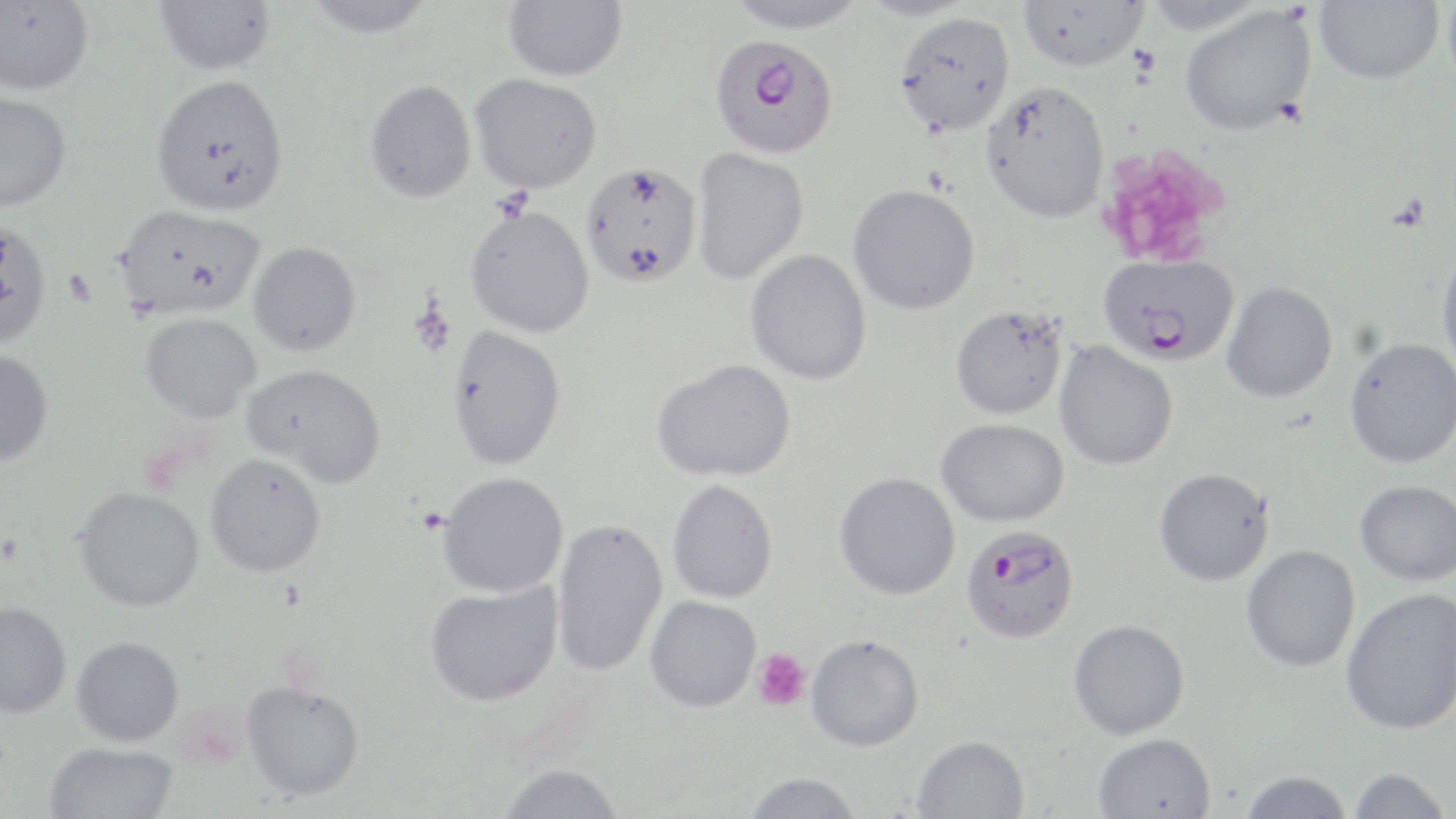

{
  "slide_level_diagnosis": "Plasmodium falciparum",
  "preparation": "thin blood smear",
  "modality": "light microscopy",
  "image_size": "1456×819 pixels",
  "plasmodium_falciparum_infected_red_blood_cell_locations": "approximate bounding boxes as (x1, y1, x2, y2) in pixels: (709, 34, 840, 159), (1098, 253, 1239, 365), (960, 524, 1080, 644)",
  "stain": "May-Grünwald-Giemsa",
  "platelet_locations": "approximate bounding boxes as (x1, y1, x2, y2) in pixels: (1098, 144, 1231, 270), (752, 648, 811, 712)",
  "uninfected_red_blood_cell_locations": "approximate bounding boxes as (x1, y1, x2, y2) in pixels: (154, 0, 275, 76), (302, 0, 436, 39), (503, 0, 627, 81), (724, 0, 869, 33), (855, 0, 979, 21), (1018, 0, 1149, 72), (1142, 0, 1267, 35), (1442, 0, 1456, 97), (0, 1, 94, 96), (1314, 1, 1444, 85), (1179, 5, 1316, 136), (893, 11, 1016, 135), (470, 73, 603, 193), (149, 74, 289, 218), (364, 80, 476, 203), (980, 81, 1110, 223), (0, 90, 72, 212), (691, 147, 809, 285), (580, 162, 703, 288), (847, 184, 981, 315), (114, 205, 265, 320), (464, 205, 595, 338), (0, 218, 53, 350), (248, 241, 360, 356), (1436, 244, 1456, 373), (745, 249, 871, 385), (1221, 282, 1338, 403), (950, 305, 1068, 420), (139, 312, 261, 422), (446, 326, 566, 471), (1343, 338, 1456, 469), (1054, 342, 1178, 471), (0, 349, 53, 466), (652, 359, 796, 482), (242, 364, 386, 488), (936, 418, 1069, 527), (205, 454, 326, 578), (1153, 468, 1274, 586), (834, 472, 960, 600), (437, 473, 569, 598), (667, 479, 779, 604), (1355, 480, 1456, 586), (74, 487, 205, 612), (551, 518, 667, 677), (1240, 545, 1360, 672), (424, 581, 563, 707), (1340, 587, 1456, 735), (645, 596, 761, 712), (0, 600, 72, 718), (1068, 619, 1190, 740), (805, 634, 923, 751), (71, 636, 184, 746), (240, 681, 365, 802), (1093, 732, 1216, 819), (912, 735, 1030, 819), (43, 742, 179, 819), (497, 763, 625, 819), (1348, 767, 1451, 819), (1239, 770, 1352, 818), (742, 773, 864, 819)",
  "magnification": "1000x",
  "field_of_view": "one of a larger specimen"
}